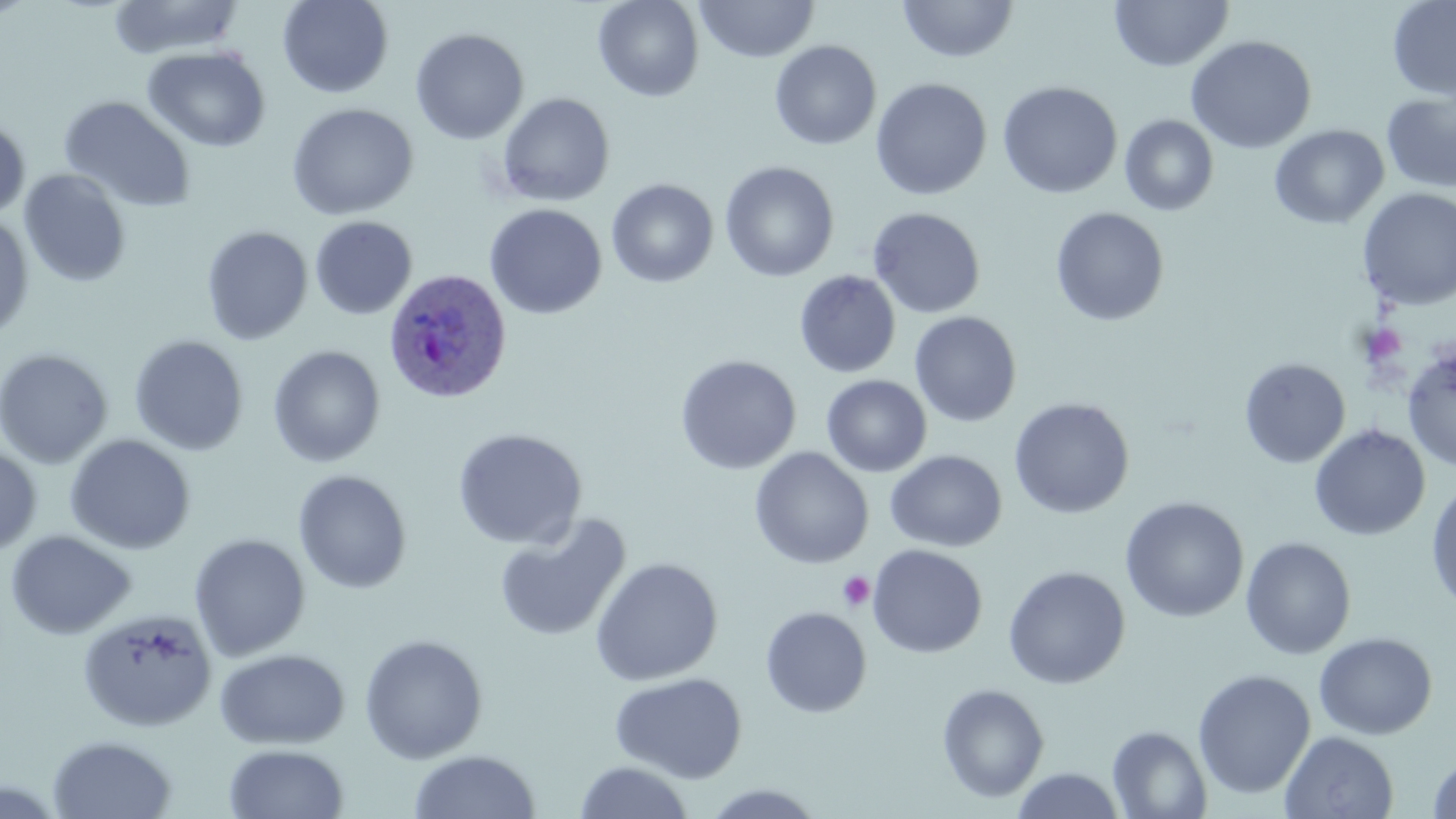

Plasmodium ovale-infected red blood cell locations = approximate bounding boxes as [x1, y1, x2, y2] in pixels: [384, 268, 512, 404]
slide-level diagnosis = Plasmodium ovale
uninfected red blood cell locations = approximate bounding boxes as [x1, y1, x2, y2] in pixels: [107, 0, 244, 60], [278, 0, 394, 99], [593, 0, 704, 102], [695, 0, 820, 62], [897, 0, 1019, 64], [1109, 0, 1234, 73], [1387, 0, 1456, 101], [410, 27, 529, 144], [1185, 35, 1318, 154], [769, 40, 882, 150], [142, 46, 271, 153], [870, 78, 992, 200], [997, 81, 1123, 200], [1381, 90, 1456, 194], [495, 92, 616, 207], [58, 95, 197, 213], [286, 102, 419, 221], [1119, 114, 1220, 216], [0, 115, 31, 221], [1269, 124, 1389, 229], [719, 161, 839, 281], [19, 168, 132, 287], [606, 178, 719, 288], [1357, 188, 1456, 310], [485, 203, 607, 320], [867, 207, 986, 319], [1049, 207, 1170, 326], [0, 213, 34, 341], [309, 216, 417, 320], [201, 225, 313, 345], [794, 270, 901, 378], [909, 311, 1022, 427], [129, 335, 249, 456], [267, 344, 385, 468], [1402, 345, 1456, 471], [0, 348, 113, 468], [675, 354, 802, 475], [1239, 357, 1351, 468], [821, 374, 932, 477], [1008, 397, 1135, 519], [1309, 424, 1430, 541], [452, 427, 588, 550], [64, 434, 196, 554], [0, 444, 42, 559], [750, 447, 874, 569], [885, 450, 1007, 552], [292, 469, 412, 594], [1426, 478, 1456, 615], [1119, 496, 1249, 623], [493, 513, 632, 643], [5, 530, 137, 640], [189, 533, 311, 661], [1240, 537, 1357, 660], [867, 544, 988, 658], [590, 557, 723, 687], [1003, 566, 1130, 689], [760, 606, 872, 718], [77, 608, 218, 732], [1313, 632, 1438, 740], [359, 633, 488, 764], [215, 648, 350, 750], [1192, 669, 1316, 800], [611, 672, 747, 783], [936, 682, 1050, 803], [1107, 725, 1212, 818], [1279, 731, 1399, 817], [47, 734, 177, 818], [223, 743, 350, 819], [408, 749, 541, 818], [1425, 751, 1456, 818], [573, 761, 695, 819], [1010, 767, 1127, 819], [699, 784, 829, 818]
preparation = thin blood smear
magnification = 1000x
stain = May-Grünwald-Giemsa
modality = optical microscopy
field of view = single
image size = 1456×819 pixels
platelet locations = approximate bounding boxes as [x1, y1, x2, y2] in pixels: [1362, 324, 1408, 367], [838, 571, 875, 611]